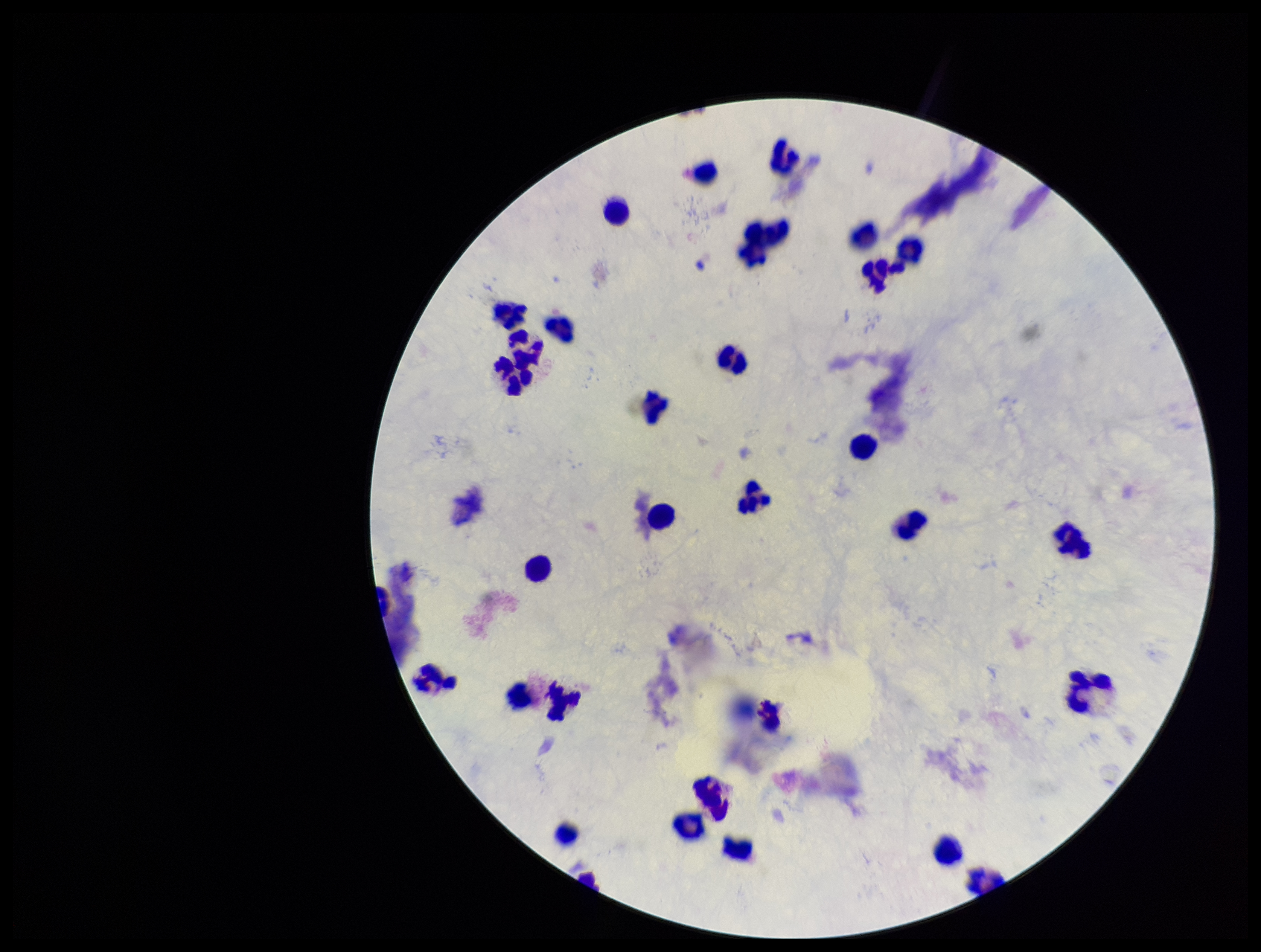
Summary:
  - Capture: smartphone photograph through the microscope eyepiece
  - Field of view: single
  - Leukocyte count: 30
  - Stain: Giemsa
  - Image size: 1261×952 pixels
  - Preparation: thick blood smear
  - Patient malaria status: negative
  - Plasmodium parasites: none identified
  - Parasite count: 0